Locate every Trypanosoma brucei.
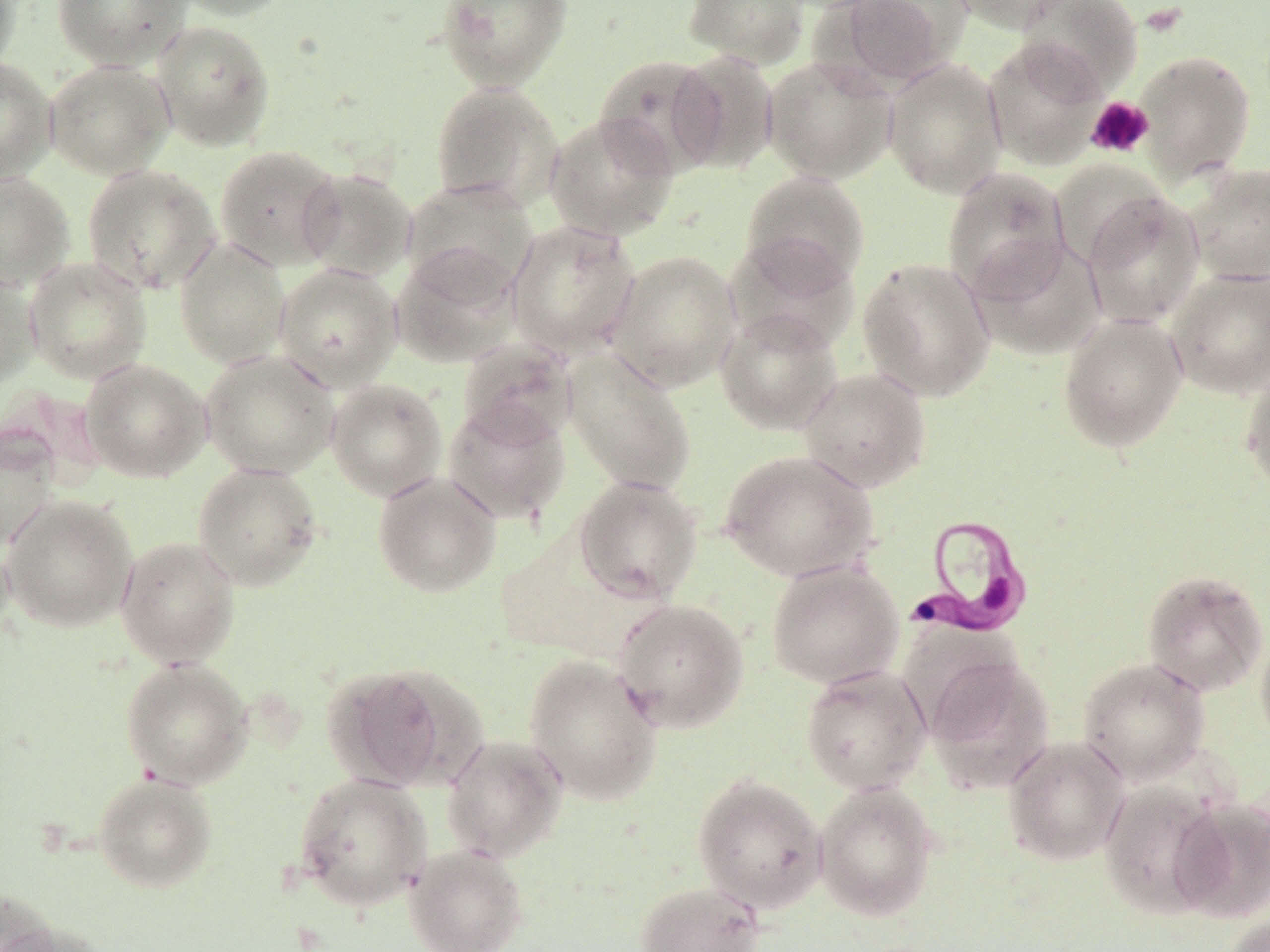
Approximate bounding boxes as (x1, y1, x2, y2) in pixels.
Trypanosoma brucei: (905, 513, 1037, 640).

Summary:
  - Platelet locations: (1085, 96, 1154, 159)
  - Uninfected red blood cell locations: (0, 0, 21, 78), (51, 0, 190, 69), (168, 0, 296, 21), (436, 0, 573, 92), (683, 0, 810, 68), (832, 0, 961, 87), (947, 0, 1078, 34), (1015, 0, 1144, 99), (150, 19, 275, 152), (983, 38, 1106, 170), (669, 50, 780, 173), (1133, 50, 1256, 183), (593, 54, 726, 178), (763, 56, 897, 183), (0, 58, 57, 185), (44, 59, 174, 180), (883, 59, 1007, 198), (429, 81, 564, 211), (544, 113, 678, 241), (214, 144, 345, 271), (1185, 162, 1270, 285), (82, 164, 222, 296), (942, 167, 1071, 302), (297, 168, 417, 282), (0, 171, 75, 292), (740, 171, 870, 290), (403, 178, 538, 298), (1081, 191, 1205, 329), (506, 219, 641, 358), (725, 235, 860, 355), (174, 237, 291, 369), (968, 238, 1106, 362), (391, 245, 522, 368), (605, 250, 741, 392), (24, 256, 152, 383), (858, 257, 995, 401), (274, 263, 402, 392), (1165, 265, 1270, 398), (0, 268, 41, 391), (714, 308, 842, 435), (1058, 312, 1189, 453), (457, 338, 578, 445), (200, 349, 340, 479), (563, 351, 696, 495), (80, 359, 211, 482), (1240, 362, 1270, 497), (798, 367, 932, 493), (326, 378, 447, 501), (442, 399, 572, 524), (0, 428, 60, 550), (719, 449, 879, 582), (192, 462, 323, 590), (372, 471, 502, 598), (573, 475, 703, 604), (1, 494, 139, 632), (116, 536, 240, 668), (0, 538, 15, 646), (766, 559, 903, 689), (1141, 569, 1269, 697), (612, 599, 750, 733), (1255, 627, 1270, 752), (923, 654, 1054, 794), (523, 655, 663, 805), (121, 657, 253, 789), (1077, 657, 1210, 785), (322, 663, 474, 791), (800, 665, 932, 795), (441, 733, 568, 862), (1003, 735, 1130, 865), (93, 772, 217, 892), (293, 773, 431, 911), (692, 773, 828, 914), (813, 781, 939, 921), (1098, 781, 1231, 919), (1170, 798, 1270, 922), (404, 844, 528, 952), (635, 881, 765, 952), (0, 886, 60, 952), (1220, 914, 1270, 952), (0, 922, 111, 952)
  - Slide-level diagnosis: Trypanosoma brucei
  - Modality: optical microscopy
  - Stain: May-Grünwald-Giemsa
  - Image size: 1270×952 pixels
  - Magnification: 1000x
  - Field of view: one of a larger specimen
  - Preparation: thin blood film